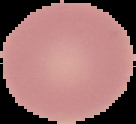

preparation: thin blood film
image_type: segmented cell region on a black background
image_size: 136×124 pixels
result: no malaria parasites seen